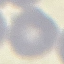

{
  "malaria_status": "uninfected",
  "stain": "Giemsa",
  "preparation": "thin blood film",
  "capture": "smartphone camera at the microscope eyepiece",
  "image_type": "automatically extracted cell patch, resized to 64 × 64 pixels"
}